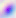

Summary:
  - Magnification: 400x
  - Modality: photomicrograph
  - Identification: Toxoplasma gondii